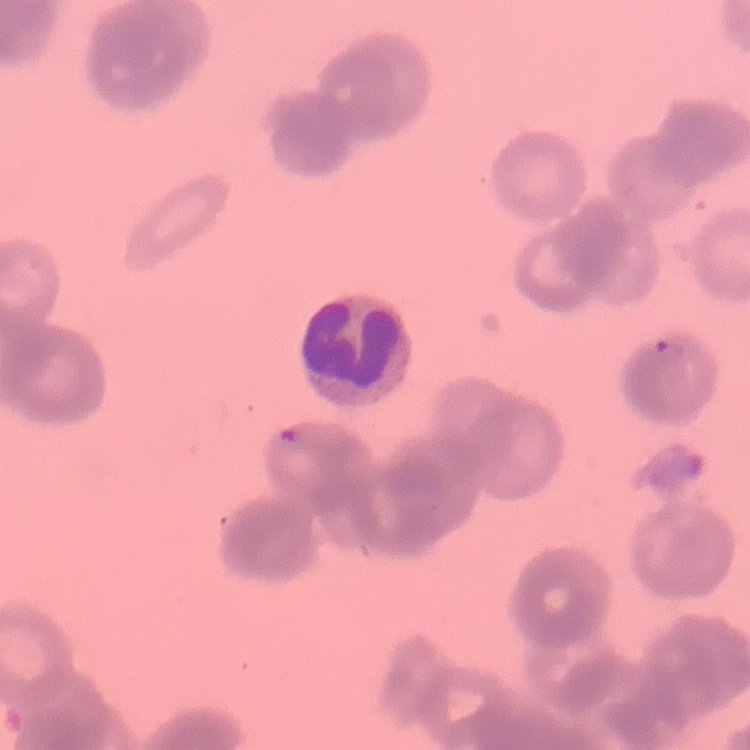
Summary:
  - Erythrocyte morphology: rouleaux formation
  - Image type: one tile cut from a larger photomicrograph
  - Stain: Field's or Giemsa
  - Preparation: thin blood smear